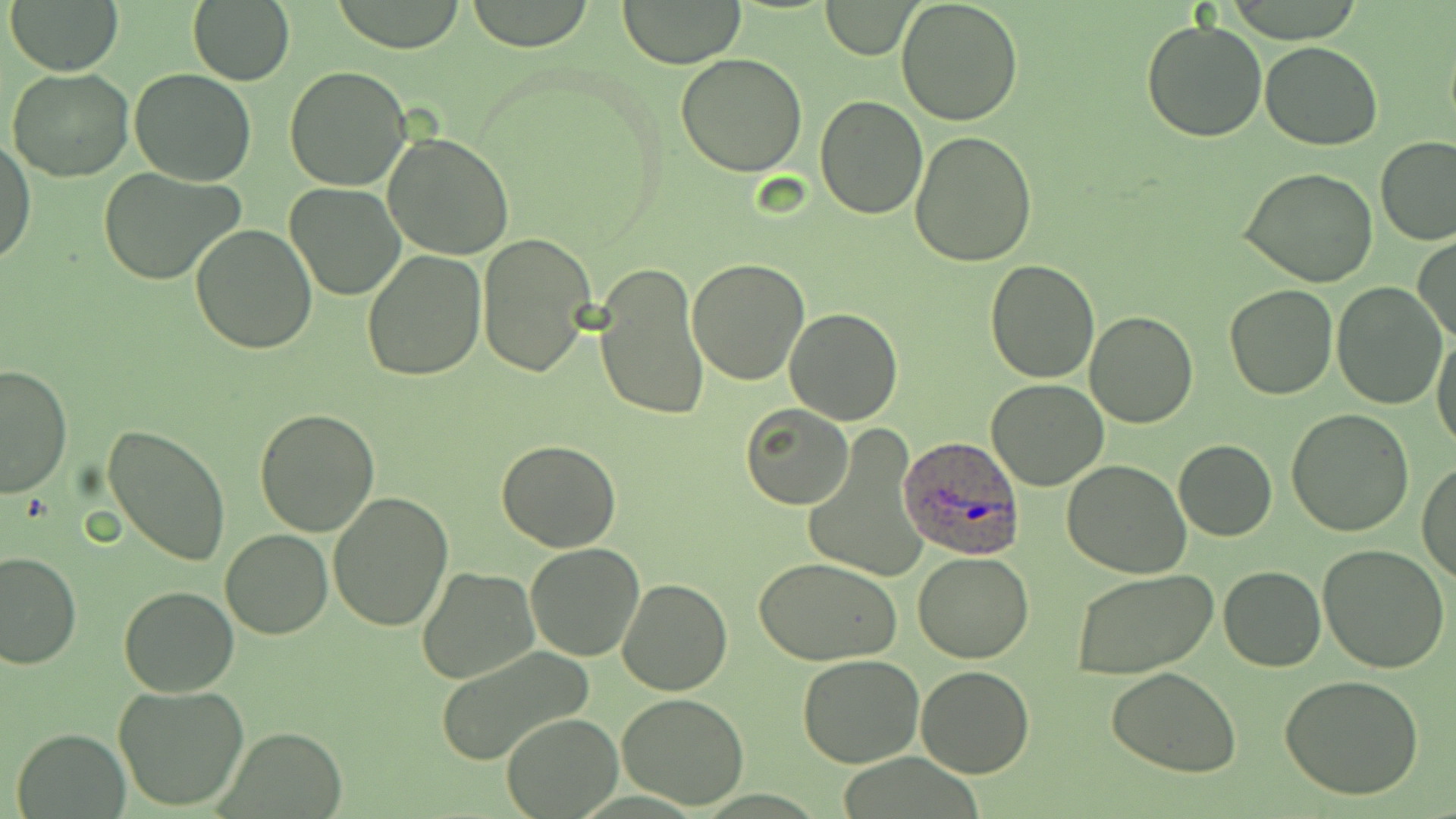

Plasmodium ovale-infected red blood cell locations = approximate bounding boxes as named x1/y1/x2/y2 corners in pixels: (x1=898, y1=437, x2=1026, y2=561)
slide-level diagnosis = Plasmodium ovale
field of view = single
modality = optical microscopy
magnification = 1000x
stain = May-Grünwald-Giemsa
uninfected red blood cell locations = approximate bounding boxes as named x1/y1/x2/y2 corners in pixels: (x1=4, y1=0, x2=125, y2=76), (x1=464, y1=0, x2=597, y2=52), (x1=896, y1=0, x2=1023, y2=125), (x1=330, y1=1, x2=468, y2=52), (x1=620, y1=1, x2=743, y2=67), (x1=822, y1=2, x2=918, y2=59), (x1=187, y1=3, x2=294, y2=84), (x1=1140, y1=18, x2=1268, y2=141), (x1=1259, y1=41, x2=1383, y2=150), (x1=676, y1=53, x2=807, y2=176), (x1=285, y1=66, x2=413, y2=191), (x1=6, y1=68, x2=133, y2=182), (x1=130, y1=68, x2=256, y2=185), (x1=812, y1=96, x2=929, y2=220), (x1=909, y1=131, x2=1037, y2=267), (x1=382, y1=132, x2=515, y2=261), (x1=1, y1=136, x2=37, y2=268), (x1=1376, y1=136, x2=1455, y2=246), (x1=97, y1=166, x2=246, y2=285), (x1=1240, y1=166, x2=1378, y2=286), (x1=284, y1=182, x2=408, y2=301), (x1=189, y1=224, x2=317, y2=354), (x1=476, y1=234, x2=595, y2=376), (x1=1414, y1=234, x2=1455, y2=344), (x1=361, y1=250, x2=487, y2=380), (x1=686, y1=258, x2=809, y2=386), (x1=985, y1=260, x2=1100, y2=384), (x1=594, y1=263, x2=709, y2=423), (x1=1331, y1=284, x2=1447, y2=409), (x1=1224, y1=286, x2=1338, y2=400), (x1=786, y1=308, x2=903, y2=424), (x1=1083, y1=309, x2=1198, y2=428), (x1=1432, y1=329, x2=1456, y2=452), (x1=0, y1=363, x2=73, y2=499), (x1=987, y1=379, x2=1109, y2=491), (x1=740, y1=403, x2=853, y2=510), (x1=254, y1=408, x2=381, y2=537), (x1=1287, y1=409, x2=1415, y2=537), (x1=103, y1=424, x2=231, y2=565), (x1=802, y1=428, x2=925, y2=586), (x1=497, y1=439, x2=620, y2=552), (x1=1173, y1=439, x2=1277, y2=540), (x1=1061, y1=459, x2=1192, y2=578), (x1=1417, y1=462, x2=1456, y2=584), (x1=327, y1=493, x2=454, y2=632), (x1=220, y1=529, x2=334, y2=640), (x1=524, y1=543, x2=645, y2=661), (x1=1317, y1=545, x2=1450, y2=672), (x1=0, y1=549, x2=81, y2=667), (x1=913, y1=550, x2=1034, y2=663), (x1=754, y1=557, x2=903, y2=667), (x1=1218, y1=566, x2=1325, y2=672), (x1=416, y1=567, x2=539, y2=685), (x1=1070, y1=570, x2=1217, y2=679), (x1=616, y1=578, x2=734, y2=696), (x1=117, y1=586, x2=238, y2=697), (x1=437, y1=647, x2=598, y2=766), (x1=797, y1=654, x2=926, y2=769), (x1=916, y1=666, x2=1035, y2=777), (x1=1106, y1=667, x2=1242, y2=778), (x1=1280, y1=674, x2=1426, y2=801), (x1=113, y1=684, x2=250, y2=813), (x1=615, y1=690, x2=750, y2=809), (x1=502, y1=712, x2=621, y2=818), (x1=219, y1=726, x2=350, y2=816), (x1=11, y1=728, x2=130, y2=816)
preparation = thin blood smear
image size = 1456×819 pixels